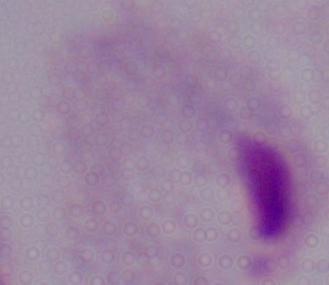

Captured at 1000x magnification. Micrograph. A trichomonad is seen.